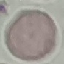
Summary:
  - Malaria status: uninfected
  - Image type: cell patch, automatically extracted from a larger field of view and resized to 64 × 64 pixels
  - Preparation: thin smear
  - Capture: smartphone camera at the microscope eyepiece
  - Stain: Giemsa